Find the red blood cells that are infected with P. falciparum, and any of indeterminate infection status.
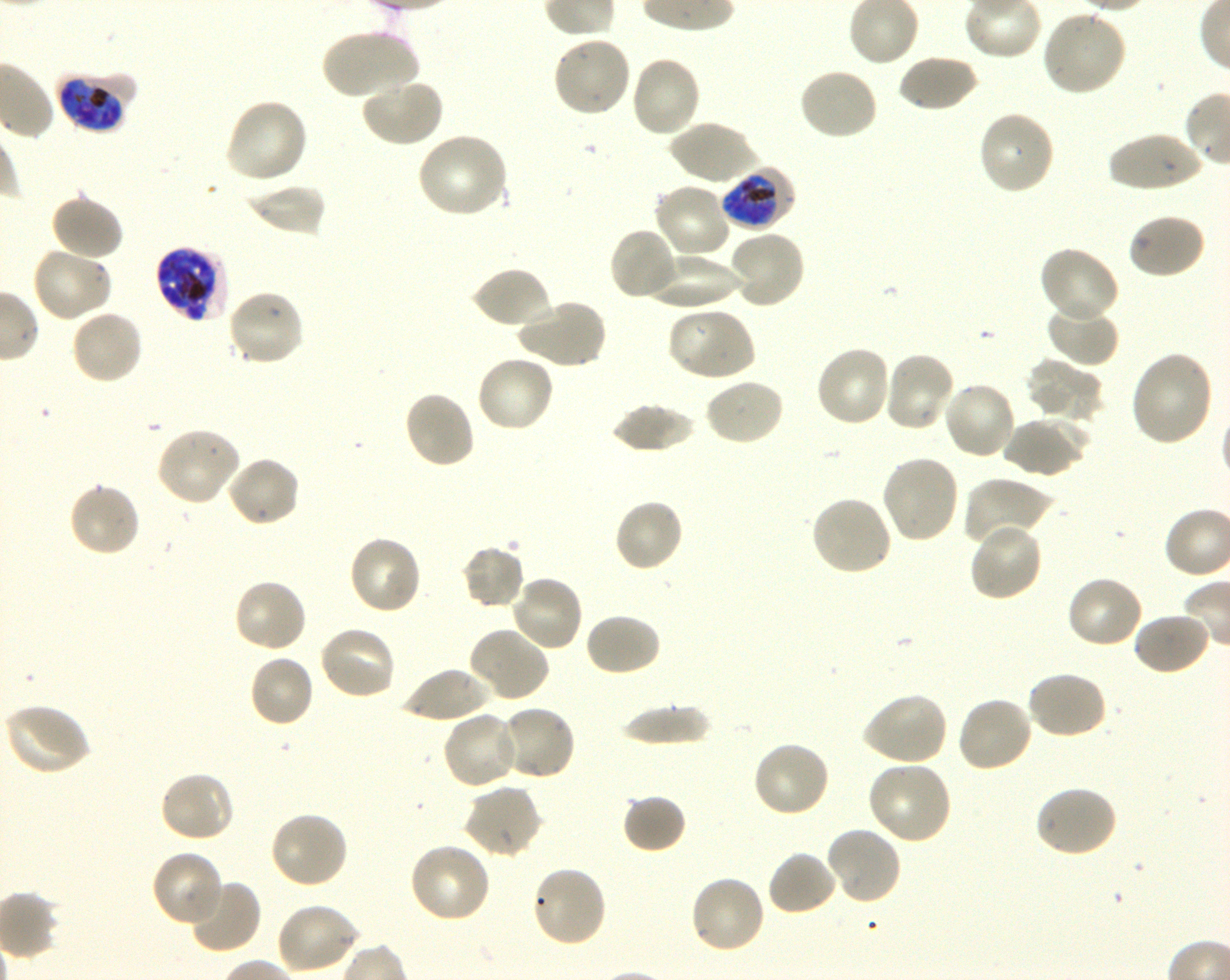
Approximate bounding rectangles given as corner coordinates in pixels from the top-left. Not every red blood cell is marked. A life-cycle stage — or a range of stages, where the recorded stages span more than one — follows each staged infected red blood cell.
Infected red blood cells: (x1=57, y1=71, x2=134, y2=133) late trophozoite to early schizont; (x1=720, y1=166, x2=795, y2=232) late trophozoite to early schizont; (x1=155, y1=246, x2=230, y2=321) late trophozoite to late schizont.
No red blood cells of indeterminate infection status observed.

Summary:
  - Locations of uninfected red blood cells: (x1=1040, y1=9, x2=1127, y2=97), (x1=320, y1=27, x2=419, y2=100), (x1=551, y1=34, x2=632, y2=118), (x1=628, y1=54, x2=702, y2=139), (x1=896, y1=55, x2=980, y2=113), (x1=797, y1=66, x2=880, y2=141), (x1=360, y1=76, x2=444, y2=148), (x1=224, y1=98, x2=309, y2=186), (x1=977, y1=109, x2=1056, y2=196), (x1=669, y1=120, x2=759, y2=187), (x1=417, y1=131, x2=510, y2=220), (x1=1106, y1=132, x2=1205, y2=192), (x1=653, y1=181, x2=732, y2=259), (x1=246, y1=183, x2=327, y2=237), (x1=50, y1=192, x2=124, y2=261), (x1=1127, y1=213, x2=1206, y2=280), (x1=609, y1=226, x2=680, y2=301), (x1=728, y1=229, x2=806, y2=309), (x1=31, y1=245, x2=113, y2=323), (x1=1038, y1=246, x2=1120, y2=323), (x1=643, y1=252, x2=741, y2=310), (x1=470, y1=266, x2=553, y2=331), (x1=226, y1=289, x2=305, y2=367), (x1=515, y1=297, x2=607, y2=371), (x1=1045, y1=300, x2=1120, y2=368), (x1=666, y1=307, x2=756, y2=383), (x1=69, y1=308, x2=144, y2=385), (x1=814, y1=345, x2=893, y2=429), (x1=1129, y1=350, x2=1213, y2=447), (x1=882, y1=351, x2=956, y2=433), (x1=475, y1=354, x2=555, y2=434), (x1=1024, y1=359, x2=1104, y2=425), (x1=703, y1=377, x2=786, y2=448), (x1=941, y1=380, x2=1018, y2=460), (x1=402, y1=389, x2=476, y2=471), (x1=611, y1=403, x2=697, y2=453), (x1=1003, y1=414, x2=1089, y2=477), (x1=155, y1=426, x2=241, y2=507), (x1=879, y1=453, x2=959, y2=545), (x1=226, y1=455, x2=301, y2=529), (x1=960, y1=478, x2=1050, y2=551), (x1=67, y1=481, x2=141, y2=558), (x1=809, y1=494, x2=893, y2=578), (x1=613, y1=497, x2=685, y2=572), (x1=968, y1=520, x2=1044, y2=603), (x1=348, y1=534, x2=424, y2=615), (x1=460, y1=544, x2=526, y2=610), (x1=510, y1=573, x2=584, y2=652), (x1=1065, y1=574, x2=1144, y2=650), (x1=232, y1=577, x2=309, y2=653), (x1=1133, y1=611, x2=1212, y2=677), (x1=585, y1=612, x2=662, y2=677), (x1=318, y1=624, x2=398, y2=701), (x1=468, y1=626, x2=551, y2=704), (x1=248, y1=654, x2=315, y2=728), (x1=398, y1=667, x2=493, y2=722), (x1=1025, y1=670, x2=1108, y2=741), (x1=860, y1=692, x2=948, y2=767), (x1=954, y1=695, x2=1034, y2=774), (x1=4, y1=702, x2=93, y2=777), (x1=619, y1=704, x2=714, y2=747), (x1=498, y1=705, x2=577, y2=781), (x1=442, y1=710, x2=520, y2=790), (x1=751, y1=740, x2=831, y2=819), (x1=867, y1=759, x2=954, y2=846), (x1=158, y1=771, x2=236, y2=844), (x1=462, y1=784, x2=544, y2=860), (x1=1032, y1=784, x2=1118, y2=858), (x1=621, y1=793, x2=687, y2=854), (x1=269, y1=810, x2=350, y2=889), (x1=824, y1=826, x2=902, y2=906), (x1=407, y1=841, x2=492, y2=925), (x1=151, y1=849, x2=224, y2=927), (x1=766, y1=849, x2=838, y2=917), (x1=530, y1=863, x2=608, y2=947), (x1=688, y1=874, x2=767, y2=955), (x1=185, y1=878, x2=262, y2=954), (x1=275, y1=902, x2=360, y2=976)
  - Donor blood group: O+
  - Preparation: thin blood smear
  - Objective: 100x, oil immersion, numerical aperture 1.30
  - Field of view: one from this slide
  - Culture: in-vitro P. falciparum strain 3D7, shaking
  - Image size: 1230×980 pixels
  - Stain: Giemsa